Assess this cell for malaria.
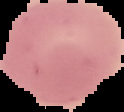

It is uninfected.

Image is 124×112 pixels. From a thin blood smear. The area outside the segmented cell region is set to black.